Outline each blood parasite and name the species.
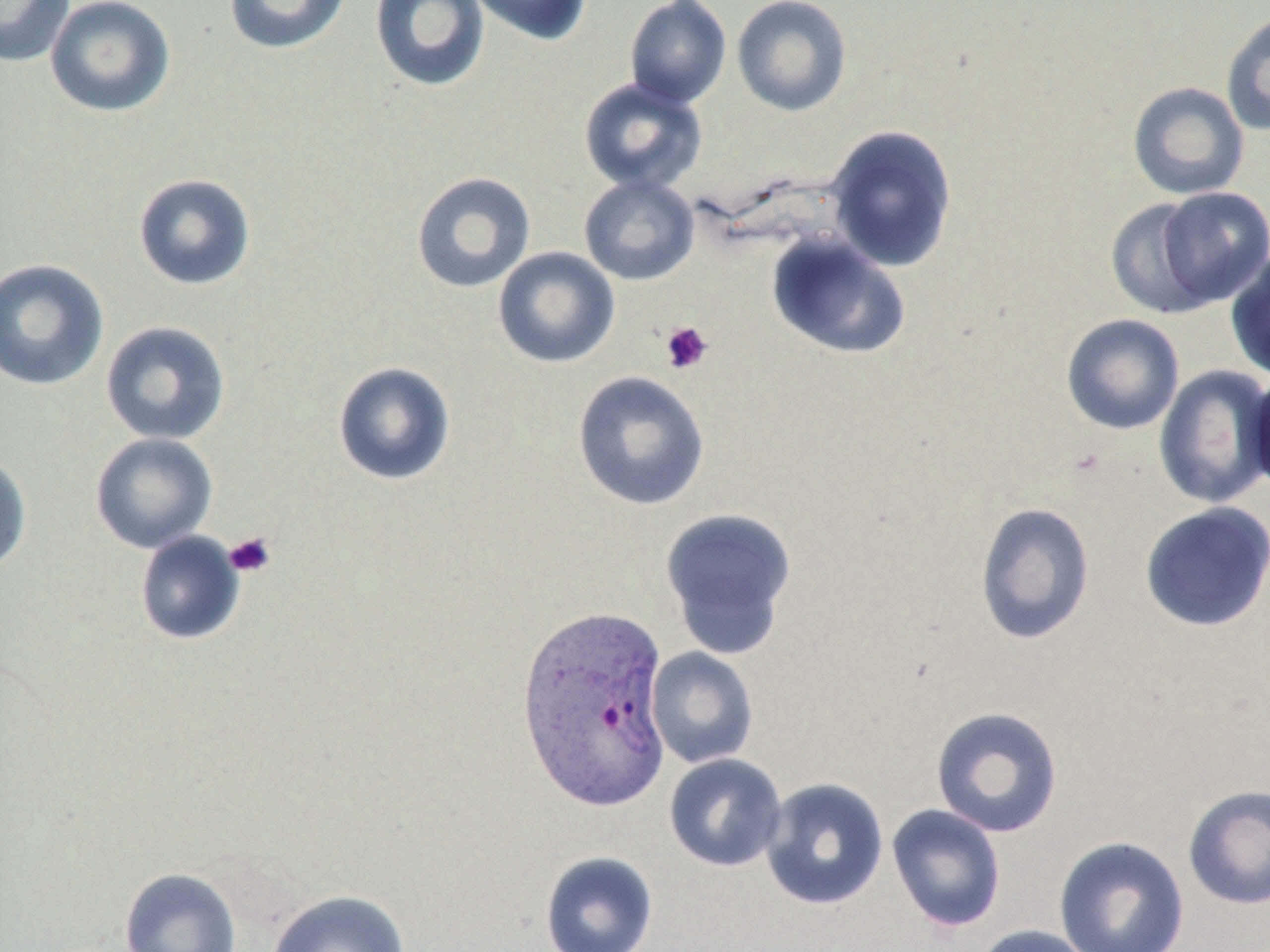

Approximate bounding boxes as (x1,y1)-(x2,y2) corner pairs in pixels.
Plasmodium ovale-infected red blood cells: (515,603)-(673,812).
No Plasmodium falciparum, Plasmodium malariae, Plasmodium vivax, Babesia divergens, or Trypanosoma brucei observed.

Summary:
  - Uninfected red blood cell locations: (0,0)-(75,67), (44,0)-(176,118), (223,0)-(352,55), (369,0)-(491,93), (466,0)-(592,46), (625,0)-(731,108), (732,0)-(852,116), (1221,10)-(1270,137), (578,77)-(708,194), (1128,82)-(1249,200), (824,124)-(958,273), (411,171)-(536,293), (133,173)-(256,291), (578,174)-(700,285), (1155,186)-(1270,309), (1105,197)-(1224,319), (765,234)-(911,360), (492,246)-(620,368), (1225,247)-(1270,382), (0,258)-(109,391), (1061,314)-(1184,435), (100,320)-(231,445), (332,360)-(456,486), (1153,364)-(1270,509), (1247,368)-(1270,499), (572,371)-(710,511), (90,433)-(218,554), (0,451)-(32,575), (975,501)-(1095,645), (1138,501)-(1270,632), (660,507)-(798,657), (134,531)-(246,646), (646,647)-(759,769), (930,705)-(1064,837), (664,753)-(788,872), (760,777)-(889,911), (1182,784)-(1270,910), (886,803)-(1006,933), (1053,835)-(1190,952), (539,850)-(659,952), (119,867)-(242,952), (266,889)-(411,952), (972,923)-(1099,952)
  - Platelet locations: (659,320)-(713,375), (223,532)-(276,578)
  - Slide-level diagnosis: Plasmodium ovale
  - Image size: 1270×952 pixels
  - Magnification: 1000x
  - Preparation: thin blood film
  - Modality: optical microscopy
  - Stain: May-Grünwald-Giemsa
  - Field of view: single